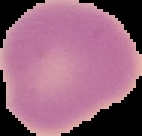
Summary:
  - Image size: 142×136 pixels
  - Image type: segmented cell region on a black background
  - Preparation: thin blood smear
  - Result: no malaria parasites seen